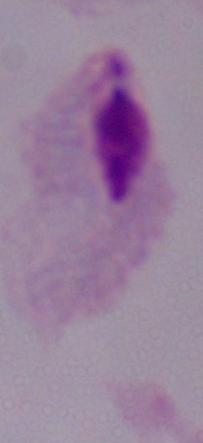
A trichomonad is shown. 1000x magnification. Micrograph.